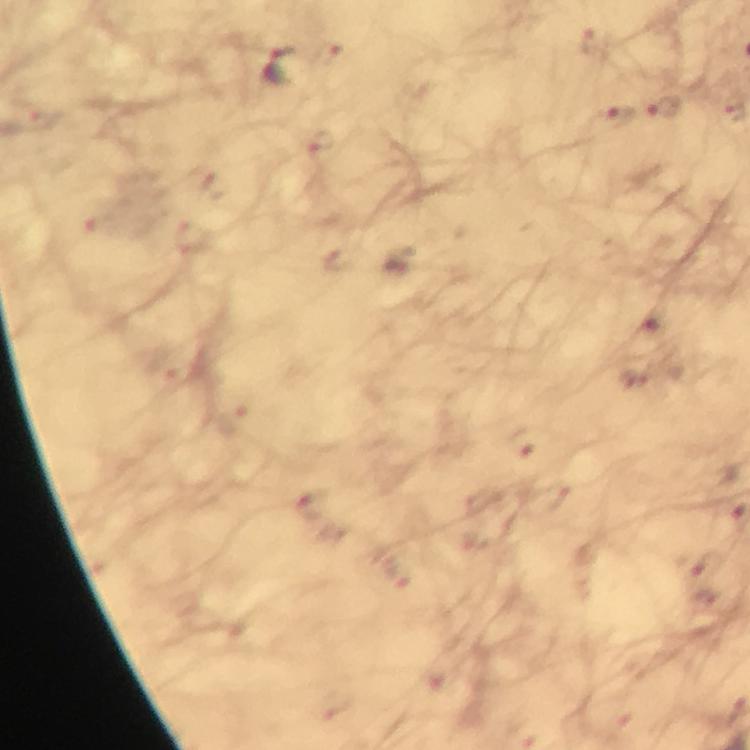
Approximate centers as {x, y} in pixels. Malaria parasite locations: {596, 42}, {327, 55}, {282, 66}, {664, 110}, {618, 116}, {42, 121}, {321, 143}, {204, 178}, {105, 228}, {195, 237}, {651, 329}, {525, 442}, {311, 504}, {709, 567}. Smartphone photograph taken through a microscope. Giemsa stain. At 100x magnification. Immersion oil was used. Image is 750×750 pixels. Cropped region of a single field of view. From a malaria diagnostic workup. Thick blood film.